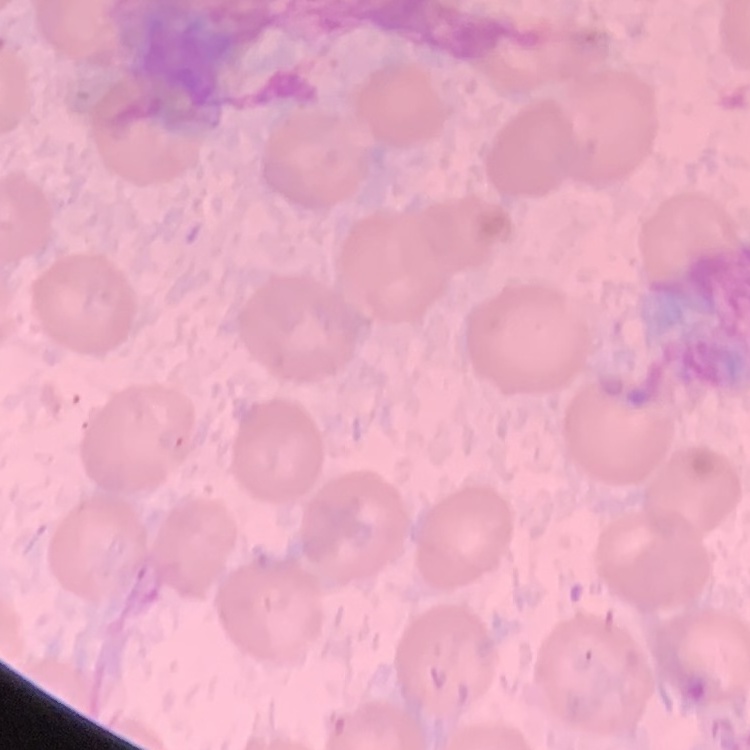

The erythrocytes show no rouleaux formation. Thin blood film. Stained with either Field's or Giemsa. Square crop of a larger photomicrograph.